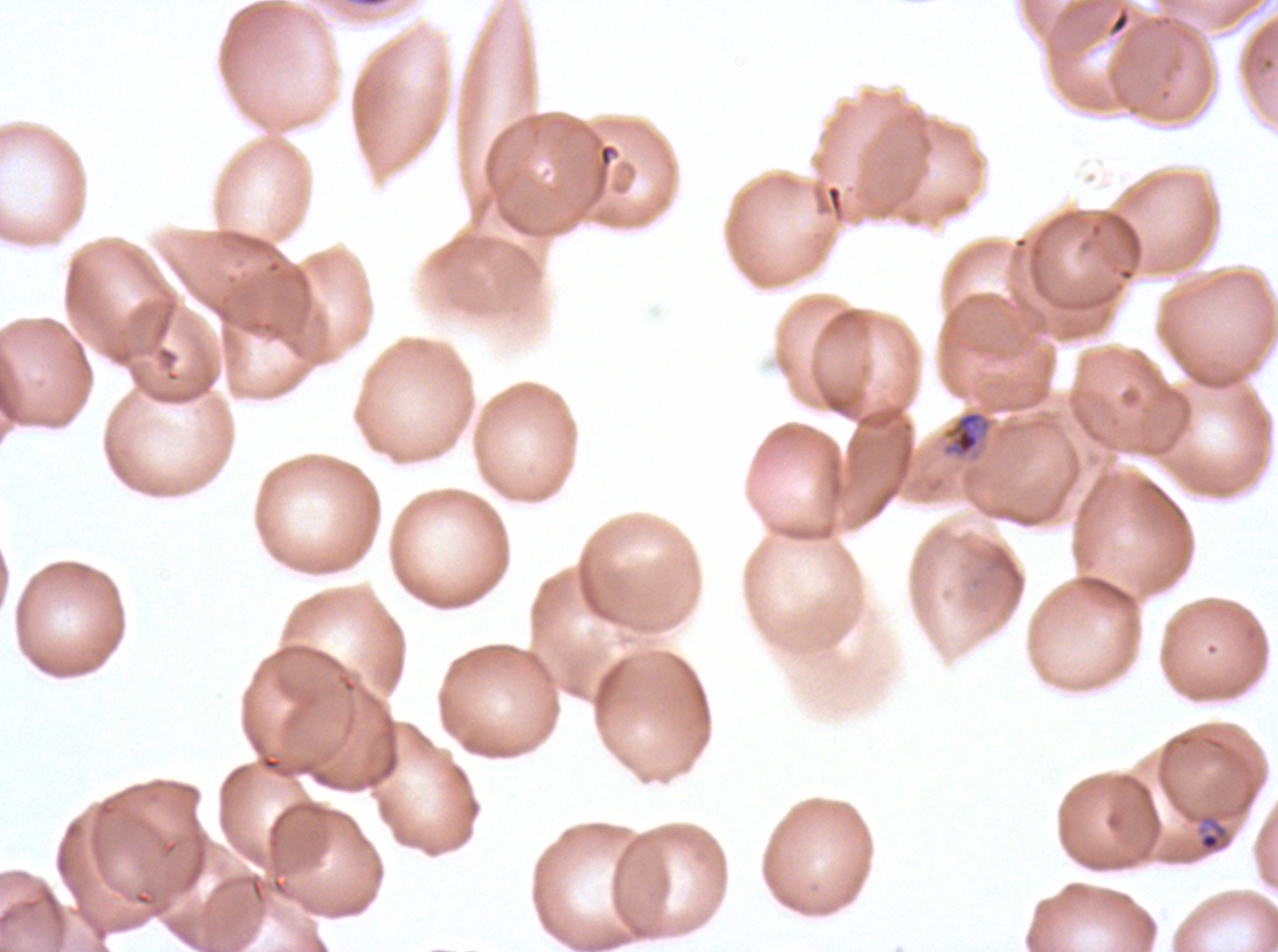
stain: Giemsa
late_ring_early_trophozoite_locations: 'approximate bounding boxes as (x1, y1, x2, y2) in pixels: (1198, 814, 1230, 853)'
mid_trophozoite_locations: 'approximate bounding boxes as (x1, y1, x2, y2) in pixels: (948, 410, 985, 458)'
image_size: 1278×952 pixels
specimen: ex-vivo Plasmodium falciparum culture from a patient in The Gambia, grown for 24 to 48 hours
life_cycle_stages_observed: late-ring/early-trophozoite, mid trophozoite
field_of_view: one sub-image of a larger composite
preparation: thin blood smear